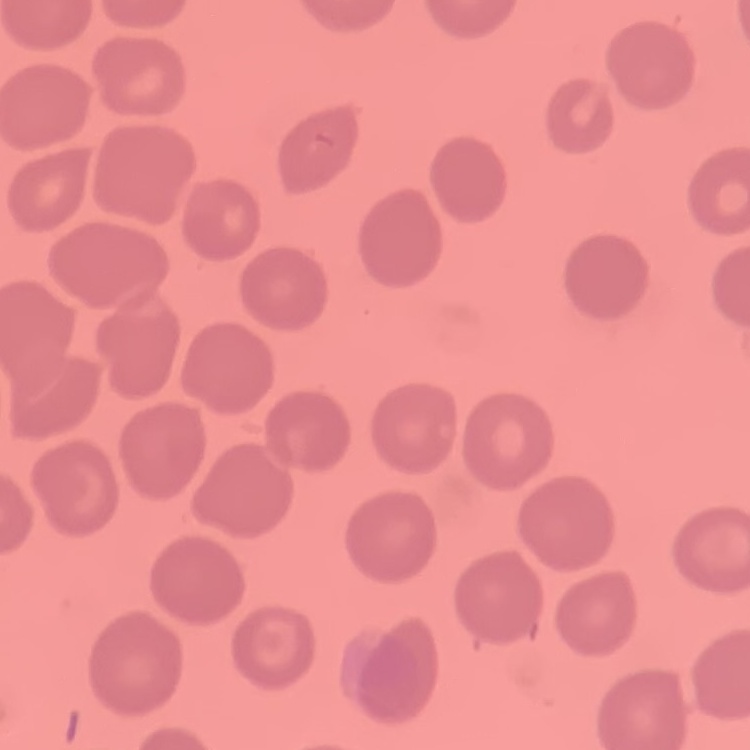

{
  "erythrocyte_morphology": "no rouleaux formation",
  "image_type": "one tile cut from a larger photomicrograph",
  "preparation": "thin blood smear",
  "stain": "Field's or Giemsa"
}